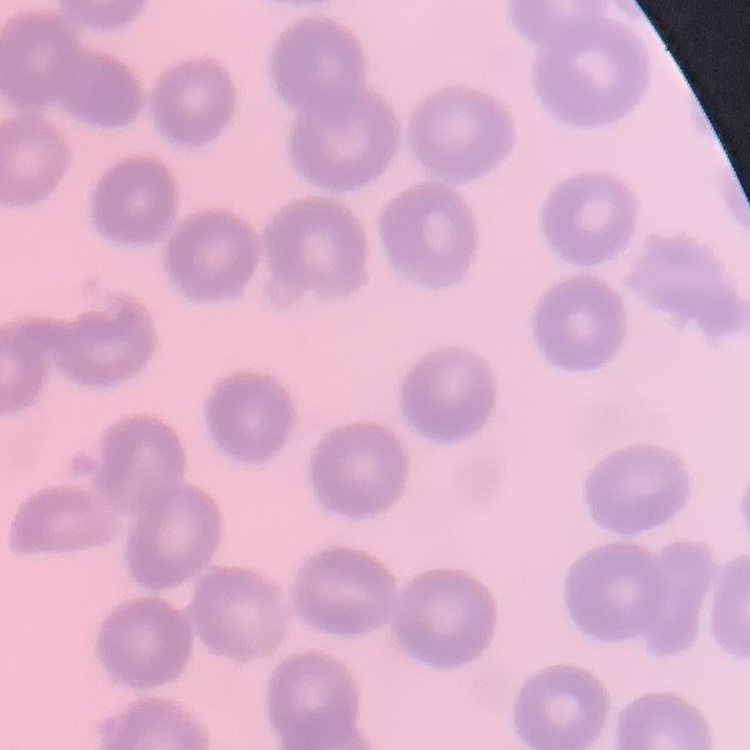

Summary:
  - Erythrocyte morphology: no rouleaux formation
  - Stain: Field's or Giemsa
  - Image type: square crop of a larger photomicrograph
  - Preparation: thin blood smear